Locate and identify every blood parasite.
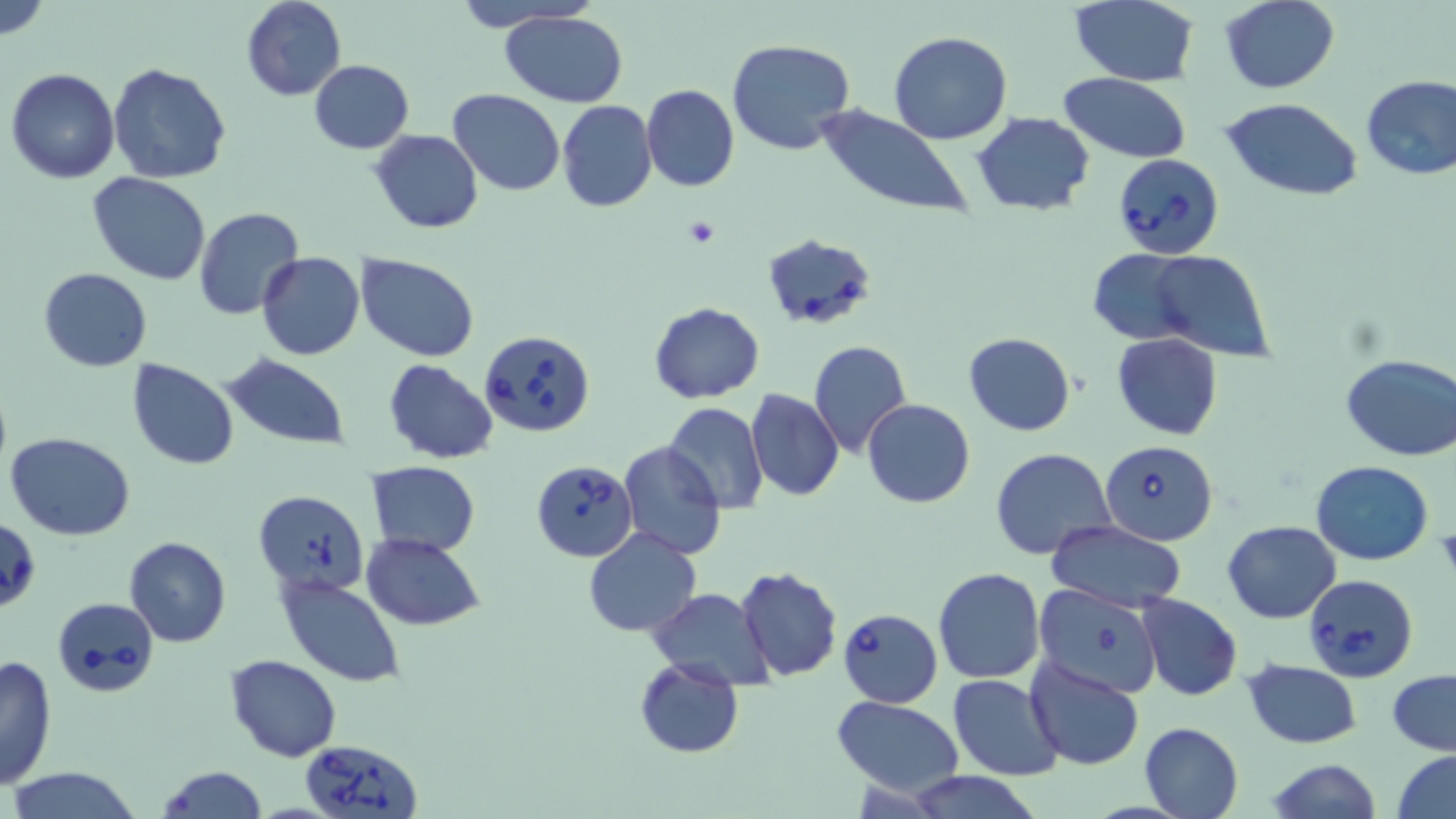
Approximate bounding boxes as [x1, y1, x2, y2] in pixels.
Babesia divergens-infected red blood cells: [1112, 152, 1226, 260], [762, 236, 876, 328], [478, 331, 596, 438], [1099, 438, 1219, 544], [531, 463, 637, 561], [254, 490, 371, 598], [1, 517, 41, 613], [1304, 573, 1418, 682], [51, 597, 159, 698], [837, 608, 942, 708], [298, 738, 424, 819].
No Plasmodium falciparum, Plasmodium ovale, Plasmodium malariae, Plasmodium vivax, or Trypanosoma brucei observed.

Platelet locations: [684, 218, 721, 248]. Uninfected red blood cell locations: [0, 0, 50, 41], [242, 0, 346, 101], [451, 0, 593, 32], [1219, 0, 1339, 93], [1070, 1, 1200, 86], [501, 10, 629, 106], [888, 31, 1014, 145], [727, 37, 856, 155], [308, 59, 414, 153], [108, 63, 231, 185], [7, 68, 121, 183], [1359, 72, 1456, 181], [1058, 73, 1190, 163], [641, 85, 739, 192], [447, 88, 564, 197], [1220, 97, 1363, 201], [557, 101, 657, 215], [812, 105, 977, 221], [971, 111, 1094, 216], [370, 128, 483, 234], [87, 170, 212, 285], [194, 208, 304, 321], [1090, 248, 1201, 343], [1146, 249, 1274, 360], [257, 252, 365, 360], [356, 253, 480, 361], [38, 267, 152, 372], [648, 303, 766, 403], [963, 333, 1075, 436], [1112, 333, 1222, 439], [809, 339, 912, 460], [219, 354, 351, 451], [1341, 355, 1456, 461], [383, 358, 499, 465], [127, 360, 239, 469], [373, 362, 489, 560], [746, 387, 844, 503], [861, 398, 975, 509], [663, 403, 768, 513], [6, 432, 135, 540], [617, 441, 727, 561], [991, 448, 1116, 561], [366, 460, 480, 558], [1311, 461, 1433, 565], [1046, 520, 1186, 611], [1223, 521, 1340, 623], [583, 526, 702, 637], [362, 532, 486, 630], [124, 537, 231, 648], [735, 567, 842, 681], [934, 567, 1046, 683], [278, 578, 403, 687], [1033, 583, 1165, 696], [649, 587, 773, 690], [1136, 593, 1242, 701], [0, 654, 57, 793], [225, 654, 342, 762], [1025, 657, 1146, 771], [633, 658, 745, 758], [1243, 660, 1362, 748], [1387, 668, 1456, 756], [949, 673, 1063, 780], [832, 696, 965, 798], [1138, 721, 1243, 819], [1392, 749, 1456, 819], [1265, 759, 1382, 818], [157, 766, 267, 819], [7, 767, 146, 819], [899, 771, 1044, 819]. Slide-level diagnosis: Babesia divergens. Image is 1456×819 pixels. Single field of view. May-Grünwald-Giemsa stain. Captured at 1000x magnification. Thin blood smear. Optical microscopy.